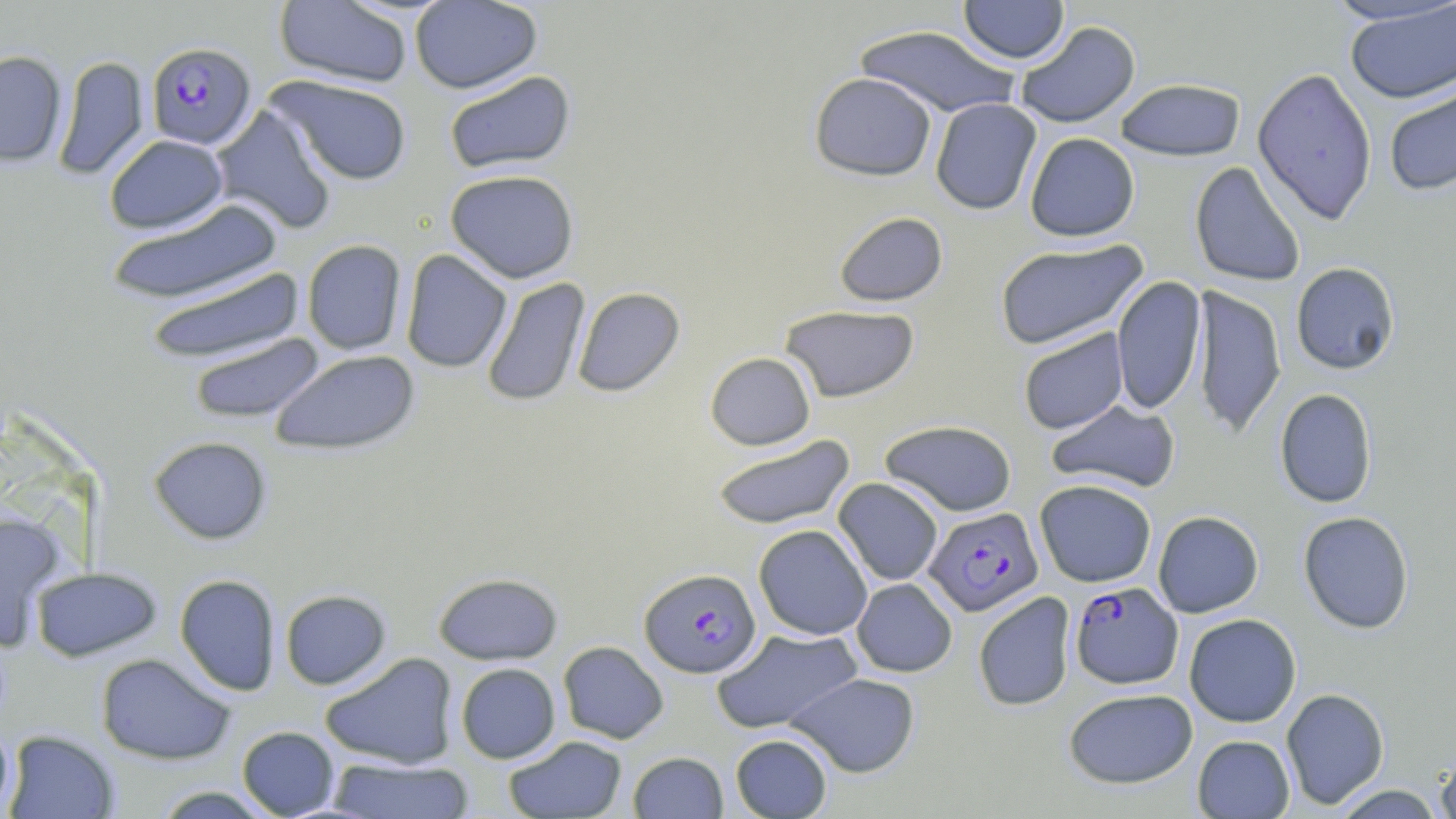
Summary:
  - Coordinate format: approximate bounding boxes as (x1,y1)-(x2,y2) corner pairs in pixels
  - Uninfected red blood cell locations: (273,0)-(412,88), (958,0)-(1069,63), (1322,0)-(1456,26), (410,1)-(542,94), (1344,1)-(1456,104), (1015,21)-(1140,129), (853,25)-(1022,118), (0,50)-(67,166), (53,55)-(149,179), (1251,67)-(1378,225), (444,70)-(576,175), (809,72)-(937,181), (266,74)-(413,186), (1115,78)-(1246,162), (1383,78)-(1456,197), (930,98)-(1042,215), (211,105)-(338,235), (1025,132)-(1140,242), (104,134)-(228,234), (1189,161)-(1306,287), (445,169)-(579,283), (106,198)-(284,305), (834,212)-(948,306), (301,239)-(407,355), (994,239)-(1149,350), (401,249)-(512,372), (1291,262)-(1400,375), (144,267)-(305,365), (1111,275)-(1207,415), (481,277)-(590,407), (1190,284)-(1287,440), (572,286)-(685,397), (780,305)-(921,403), (1018,327)-(1129,435), (189,333)-(325,424), (270,349)-(420,456), (705,352)-(816,450), (1274,388)-(1378,508), (1046,399)-(1180,494), (880,419)-(1017,516), (711,435)-(856,529), (149,436)-(273,544), (833,478)-(943,585), (1035,479)-(1157,587), (1152,510)-(1264,618), (0,511)-(67,650), (1298,511)-(1415,634), (753,524)-(872,641), (31,567)-(162,662), (433,572)-(563,665), (174,574)-(281,695), (851,578)-(957,677), (280,589)-(391,689), (973,592)-(1076,712), (1184,613)-(1301,727), (712,627)-(862,733), (558,641)-(669,744), (319,652)-(459,769), (96,653)-(236,765), (455,662)-(560,763), (786,672)-(921,777), (1063,687)-(1197,789), (1280,687)-(1389,809), (0,722)-(14,817), (237,726)-(340,817), (4,730)-(120,818), (730,734)-(832,818), (504,735)-(627,818), (1192,735)-(1294,818), (628,751)-(727,818), (1434,753)-(1456,817), (326,757)-(474,818), (1331,784)-(1446,818), (149,786)-(280,818)
  - Plasmodium falciparum-infected red blood cell locations: (146,41)-(256,149), (924,506)-(1043,617), (640,568)-(761,678), (1069,582)-(1183,689)
  - Slide-level diagnosis: Plasmodium falciparum
  - Preparation: thin blood smear
  - Image size: 1456×819 pixels
  - Stain: May-Grünwald-Giemsa
  - Field of view: one of a larger specimen
  - Magnification: 1000x
  - Modality: light microscopy